Identify the blood parasite species.
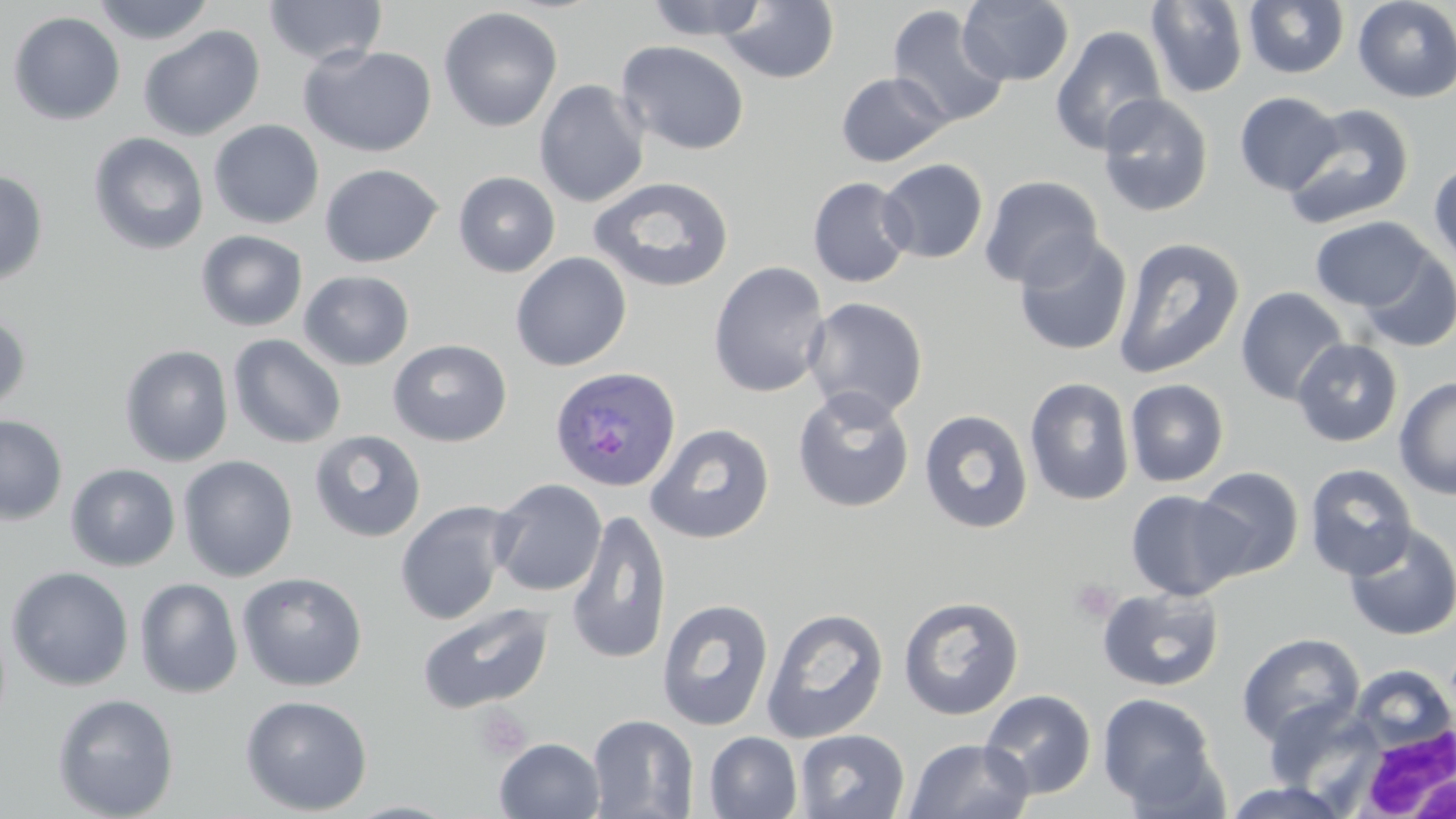

Plasmodium ovale.

Approximate bounding boxes as (x1,y1)-(x2,y2) corner pairs in pixels. Platelet locations: (1068,577)-(1121,623), (472,705)-(531,762). Uninfected red blood cell locations: (90,0)-(216,46), (263,0)-(387,67), (644,0)-(771,41), (720,0)-(840,84), (957,0)-(1075,87), (1145,0)-(1249,98), (1243,0)-(1349,79), (1353,0)-(1456,103), (886,4)-(1010,129), (438,6)-(563,133), (8,11)-(126,125), (139,24)-(265,141), (1050,24)-(1168,155), (616,40)-(750,156), (299,45)-(437,157), (835,71)-(952,168), (534,79)-(650,208), (1235,91)-(1343,195), (1097,92)-(1214,218), (1282,104)-(1415,230), (208,119)-(325,230), (88,132)-(209,256), (878,158)-(989,264), (1428,160)-(1456,271), (320,163)-(443,267), (0,169)-(49,287), (453,171)-(561,277), (587,175)-(735,294), (979,175)-(1104,290), (807,177)-(915,288), (1310,216)-(1434,311), (195,230)-(308,331), (1013,233)-(1132,357), (1112,237)-(1246,380), (1358,247)-(1456,353), (510,252)-(632,371), (708,261)-(831,398), (299,270)-(414,370), (1235,287)-(1350,406), (803,297)-(929,421), (0,310)-(32,416), (228,334)-(347,449), (1291,338)-(1404,447), (388,340)-(512,447), (119,344)-(235,467), (1024,376)-(1134,506), (1394,377)-(1456,500), (1124,378)-(1230,487), (792,387)-(915,513), (918,408)-(1034,534), (0,414)-(68,526), (645,422)-(775,543), (309,429)-(427,543), (178,455)-(298,582), (65,463)-(181,571), (1304,463)-(1417,580), (1192,466)-(1305,579), (490,478)-(607,597), (1125,489)-(1250,601), (394,501)-(515,626), (566,508)-(672,666), (1342,522)-(1456,641), (5,566)-(134,692), (237,571)-(368,691), (134,578)-(243,699), (1096,586)-(1225,693), (897,594)-(1025,720), (657,598)-(775,732), (416,603)-(554,715), (761,607)-(890,744), (1236,632)-(1365,747), (1349,664)-(1455,755), (980,689)-(1097,800), (1097,692)-(1218,808), (52,693)-(179,819), (239,694)-(373,816), (1262,699)-(1381,797), (587,714)-(699,818), (794,729)-(910,818), (704,731)-(802,819), (494,737)-(605,819), (904,737)-(1034,819), (1221,781)-(1352,819), (343,800)-(465,819). Plasmodium ovale-infected red blood cell locations: (549,365)-(681,492). White blood cell locations: (1351,726)-(1456,819). May-Grünwald-Giemsa stain. Thin blood film. Optical microscopy. 1000x magnification. Image is 1456×819 pixels. One field of a larger specimen.